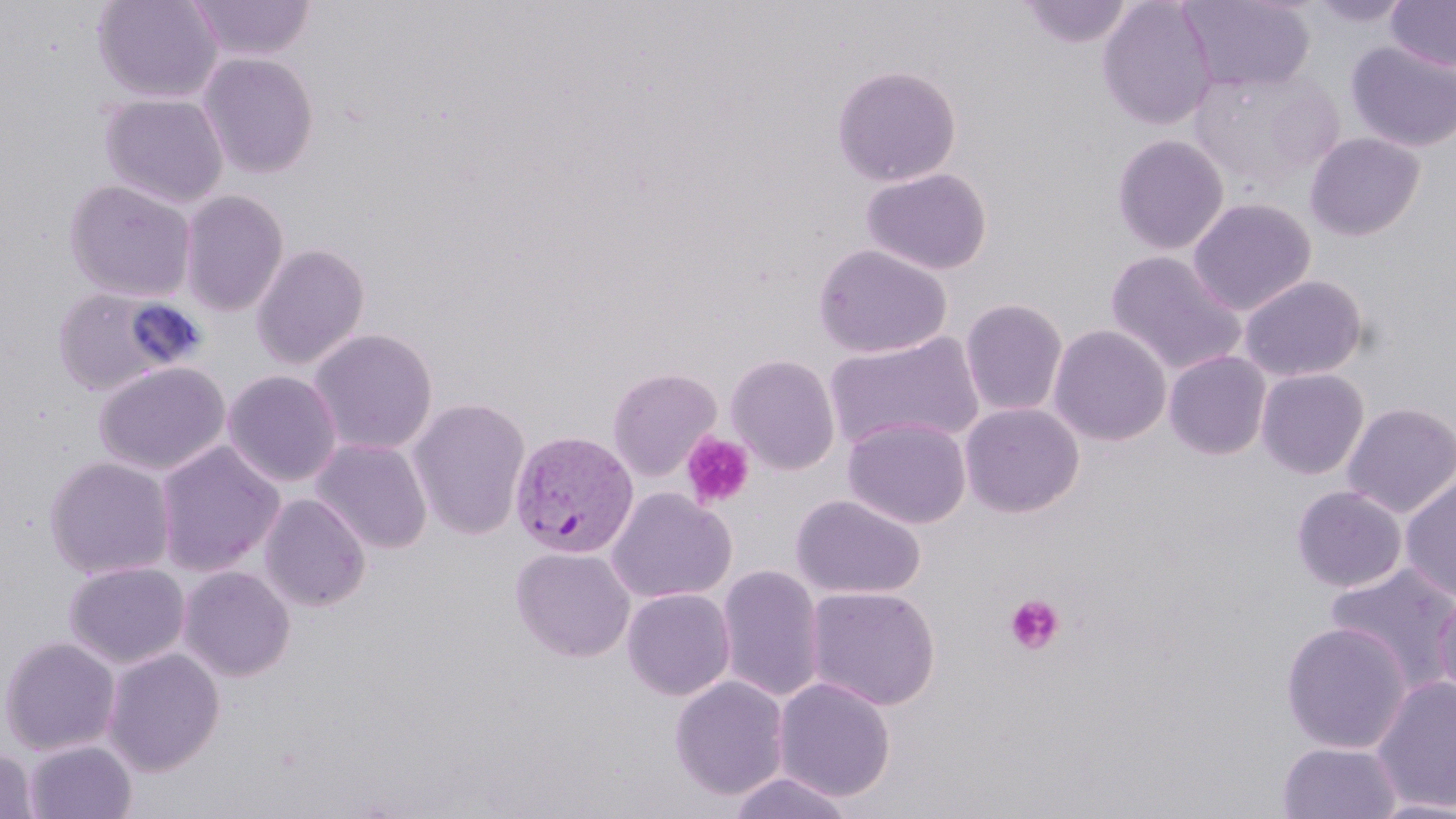

Summary:
  - Coordinate format: approximate bounding boxes as [x1, y1, x2, y2] in pixels
  - Plasmodium vivax-infected red blood cell locations: [508, 430, 639, 559]
  - Uninfected red blood cell locations: [92, 0, 224, 104], [187, 0, 316, 62], [1097, 0, 1217, 130], [1182, 0, 1315, 92], [1305, 0, 1415, 27], [1386, 0, 1456, 72], [1019, 1, 1134, 48], [1347, 41, 1456, 152], [197, 51, 320, 179], [831, 64, 962, 187], [1188, 67, 1341, 189], [99, 93, 229, 209], [1304, 132, 1426, 241], [1112, 134, 1229, 255], [861, 168, 992, 275], [63, 179, 197, 302], [178, 190, 289, 317], [1187, 198, 1316, 316], [250, 242, 371, 370], [813, 243, 952, 358], [1106, 250, 1246, 376], [1239, 274, 1368, 382], [51, 285, 187, 396], [960, 298, 1068, 417], [1048, 324, 1171, 446], [308, 328, 438, 455], [824, 332, 984, 453], [1164, 350, 1272, 460], [725, 354, 840, 475], [94, 361, 231, 476], [606, 367, 722, 481], [1255, 368, 1369, 479], [222, 370, 342, 487], [408, 397, 531, 540], [960, 402, 1084, 517], [1342, 402, 1456, 517], [843, 417, 971, 529], [311, 438, 433, 554], [154, 440, 285, 578], [43, 456, 176, 580], [1400, 476, 1456, 600], [1291, 485, 1407, 593], [605, 487, 737, 603], [259, 493, 372, 612], [790, 494, 926, 600], [510, 547, 636, 663], [63, 561, 190, 669], [1324, 562, 1456, 693], [716, 564, 825, 702], [178, 565, 296, 682], [1432, 584, 1456, 705], [804, 585, 941, 711], [622, 588, 736, 701], [1280, 622, 1412, 754], [0, 635, 121, 756], [102, 647, 226, 775], [669, 676, 790, 801], [1371, 676, 1456, 812], [774, 677, 895, 802], [23, 739, 137, 819], [1277, 741, 1403, 819], [0, 747, 39, 819], [727, 771, 857, 818], [1366, 797, 1456, 819]
  - Platelet locations: [681, 432, 754, 510], [1004, 595, 1065, 655]
  - Slide-level diagnosis: Plasmodium vivax
  - Field of view: one of a larger specimen
  - Stain: May-Grünwald-Giemsa
  - Preparation: thin blood film
  - Modality: optical microscopy
  - Magnification: 1000x
  - Image size: 1456×819 pixels